Point out malaria parasites and leukocytes.
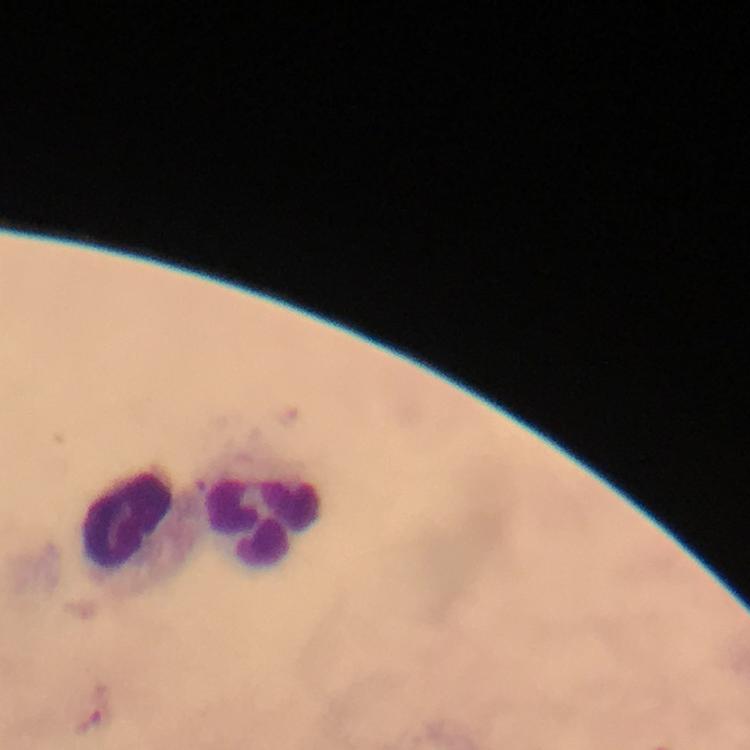
Approximate centers as {x, y} in pixels.
Malaria parasites: {88, 724}.
Leukocytes: {264, 503}, {128, 526}.

preparation = thick smear
immersion oil = used
context = from a malaria diagnostic workup
capture = smartphone mounted on the microscope
magnification = 100x
image size = 750×750 pixels
stain = Giemsa
cropped from = one field of view